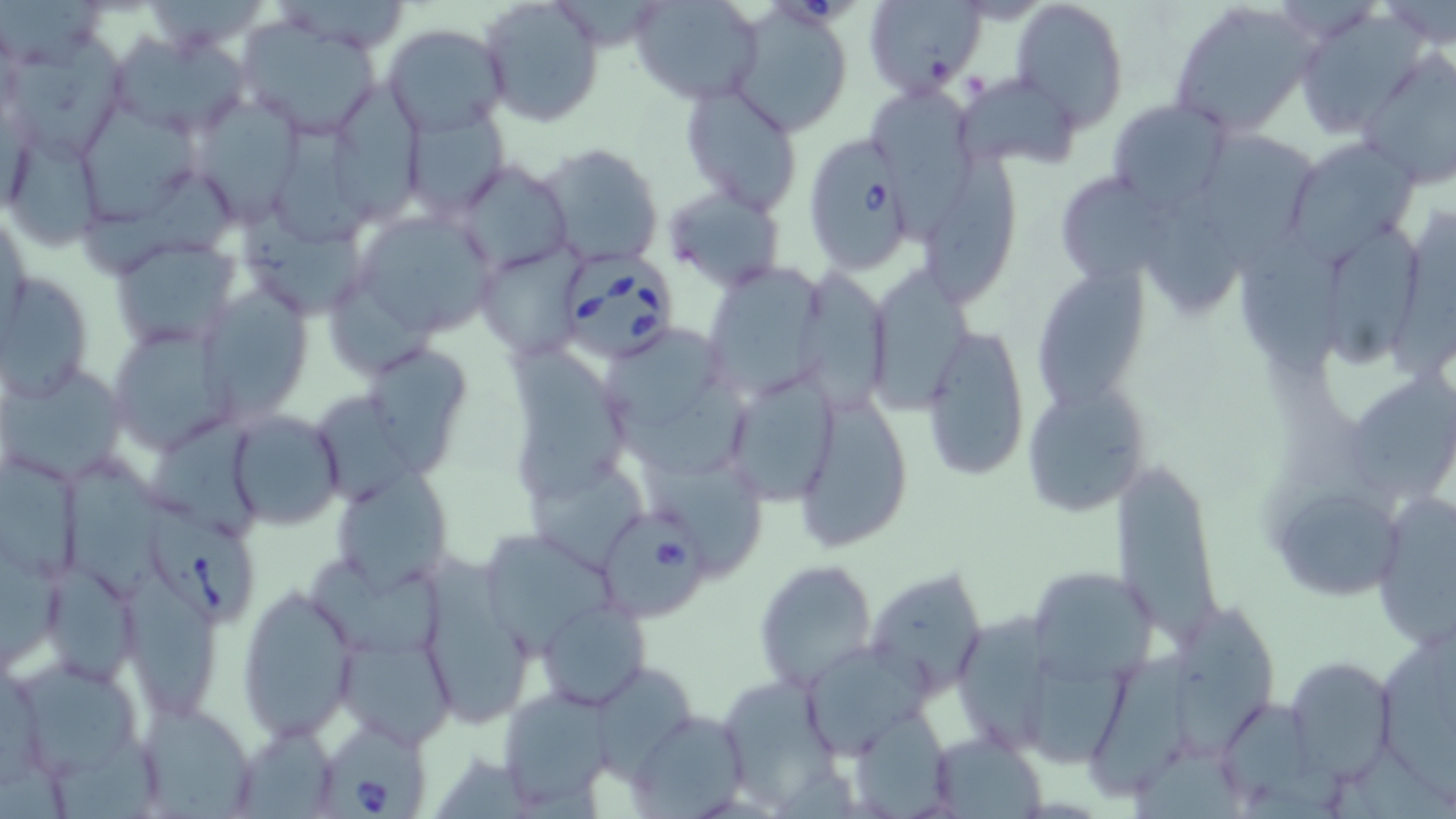
{
  "slide_level_diagnosis": "Babesia divergens",
  "image_size": "1456×819 pixels",
  "field_of_view": "one of a larger specimen",
  "uninfected_red_blood_cell_locations": "approximate bounding boxes as [x1, y1, x2, y2] in pixels: [477, 0, 604, 126], [631, 0, 766, 106], [864, 0, 987, 97], [1012, 0, 1130, 128], [0, 1, 111, 77], [279, 1, 418, 56], [562, 1, 660, 54], [1167, 2, 1321, 137], [1295, 8, 1428, 137], [238, 20, 386, 137], [383, 23, 511, 135], [726, 23, 849, 153], [109, 28, 252, 139], [6, 33, 125, 163], [1360, 55, 1456, 189], [957, 72, 1083, 171], [332, 78, 425, 224], [679, 82, 803, 215], [872, 83, 975, 244], [191, 93, 305, 227], [1107, 99, 1232, 209], [403, 110, 509, 220], [83, 112, 203, 226], [9, 125, 102, 252], [1203, 127, 1322, 277], [275, 128, 376, 250], [1286, 139, 1421, 260], [539, 143, 663, 267], [924, 155, 1020, 311], [453, 161, 574, 273], [1055, 171, 1175, 288], [90, 173, 234, 282], [664, 185, 786, 291], [1151, 194, 1253, 317], [346, 205, 500, 350], [247, 210, 367, 321], [1387, 211, 1456, 388], [1238, 227, 1357, 377], [1330, 229, 1423, 372], [109, 236, 240, 350], [1040, 264, 1150, 418], [703, 269, 824, 400], [793, 270, 890, 417], [869, 271, 979, 409], [0, 272, 95, 402], [199, 278, 316, 426], [327, 279, 439, 376], [104, 319, 236, 449], [918, 320, 1030, 480], [608, 331, 720, 431], [510, 344, 626, 499], [374, 353, 474, 478], [1, 365, 127, 483], [722, 365, 843, 508], [1352, 372, 1456, 502], [1021, 383, 1151, 519], [618, 387, 760, 485], [321, 393, 423, 505], [802, 403, 914, 555], [224, 411, 344, 529], [1113, 453, 1224, 649], [1, 456, 83, 586], [644, 461, 764, 575], [66, 462, 172, 602], [526, 463, 650, 569], [330, 469, 453, 593], [1279, 486, 1404, 596], [1366, 496, 1453, 648], [481, 535, 616, 667], [0, 550, 61, 673], [421, 557, 534, 733], [753, 559, 879, 691], [312, 562, 449, 657], [864, 570, 991, 700], [47, 571, 140, 689], [127, 572, 222, 720], [1030, 574, 1163, 686], [237, 586, 358, 742], [536, 601, 649, 708], [1178, 603, 1277, 761], [957, 612, 1053, 752], [1375, 636, 1456, 804], [337, 637, 456, 745], [801, 639, 934, 761], [1020, 648, 1133, 765], [1091, 650, 1211, 804], [1286, 656, 1396, 780], [14, 657, 145, 777], [595, 671, 695, 783], [722, 673, 837, 801], [498, 690, 621, 811], [137, 702, 260, 816], [1223, 706, 1354, 812], [624, 707, 749, 817], [861, 710, 951, 817], [234, 727, 341, 817], [931, 729, 1050, 817], [59, 730, 158, 819], [1331, 741, 1454, 819], [1131, 743, 1242, 819]",
  "preparation": "thin blood film",
  "magnification": "1000x",
  "stain": "May-Grünwald-Giemsa",
  "modality": "optical microscopy",
  "babesia_divergens_infected_red_blood_cell_locations": "approximate bounding boxes as [x1, y1, x2, y2] in pixels: [770, 0, 857, 26], [813, 147, 910, 273], [559, 249, 679, 364], [143, 506, 257, 624], [604, 519, 709, 623], [326, 722, 427, 819]"
}